Locate cells.
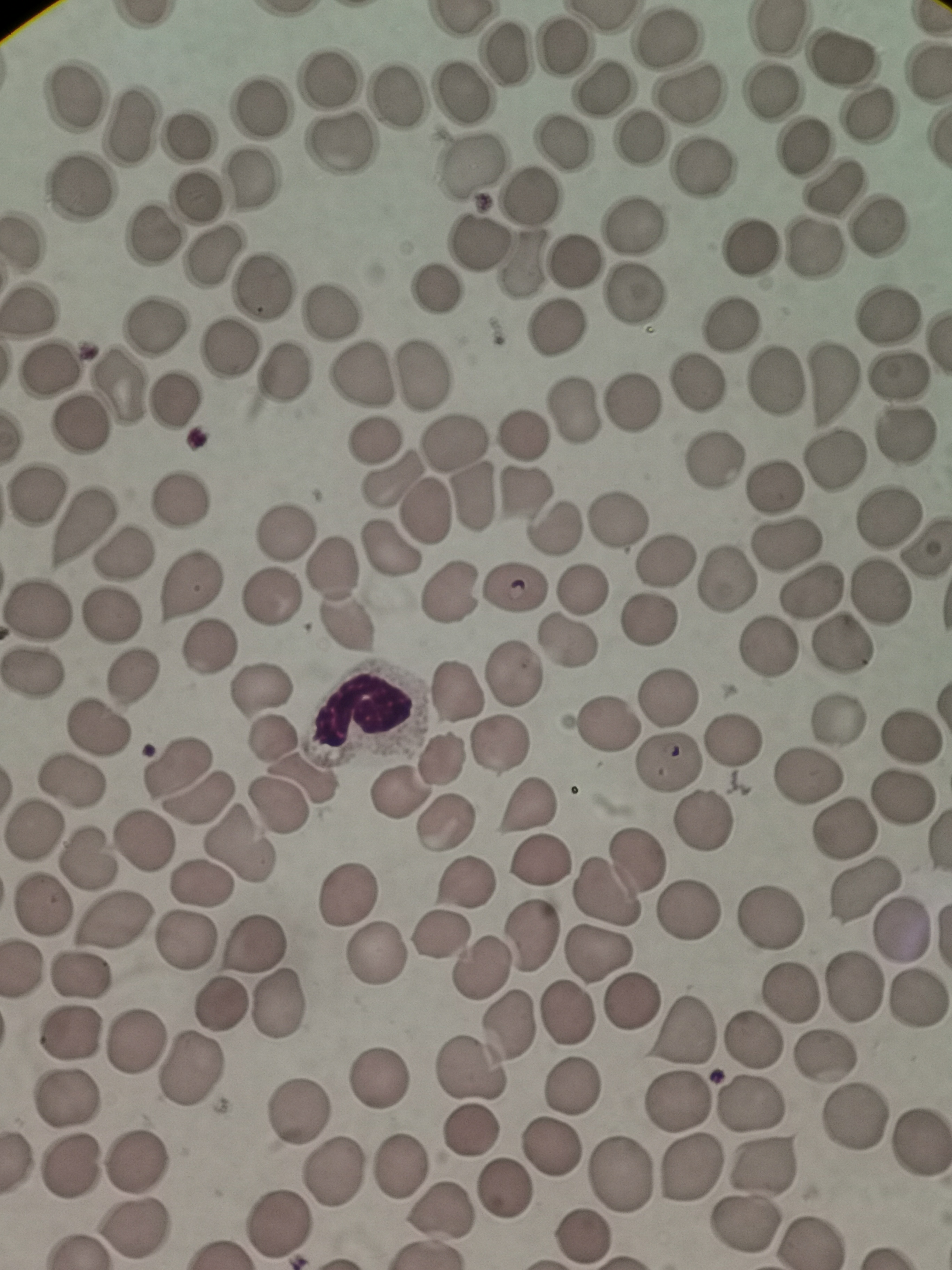
Approximate centers as (x, y) in pixels.
Cells: (775, 30), (665, 38), (564, 46), (507, 55), (842, 56), (330, 84), (605, 88), (772, 90), (399, 92), (467, 93), (694, 97), (78, 100), (264, 111), (871, 114), (130, 129), (637, 134), (193, 135), (340, 144), (563, 144), (801, 148), (473, 164), (702, 170), (253, 182), (82, 187), (833, 190), (530, 194), (199, 195), (634, 227), (880, 228), (150, 235), (483, 240), (750, 252), (817, 252), (210, 257), (575, 261), (525, 263), (259, 283), (433, 289), (631, 297), (29, 309), (334, 312), (886, 317), (155, 325), (731, 325), (558, 326), (228, 349), (53, 364), (424, 372), (280, 375), (897, 376), (362, 377), (774, 382), (831, 383), (696, 385), (118, 388), (175, 396), (629, 403), (572, 410), (80, 423), (903, 432), (523, 434), (453, 440), (372, 444), (833, 461), (714, 464), (392, 483), (776, 485), (474, 490), (32, 491), (181, 493), (523, 497), (426, 510), (887, 514), (618, 520), (85, 521), (559, 523), (286, 528), (786, 546), (390, 548), (926, 550), (126, 554), (336, 558), (667, 559), (727, 576), (185, 586), (582, 586), (515, 588), (812, 590), (449, 593), (881, 595), (273, 597), (38, 609), (109, 618), (651, 621), (348, 623), (565, 639), (844, 641), (208, 647), (763, 649), (34, 672), (514, 675), (134, 681), (259, 688), (459, 690), (666, 696), (835, 717), (606, 723), (99, 727), (272, 736), (913, 736), (732, 738), (497, 743), (439, 759), (669, 760), (174, 765), (806, 774), (303, 777), (73, 781), (397, 795), (901, 797), (200, 799), (527, 805), (280, 808), (705, 818), (448, 821), (842, 826), (35, 831), (145, 843), (242, 846), (87, 857), (543, 860), (620, 872), (464, 880), (202, 885), (864, 889), (346, 899), (43, 907), (685, 912), (771, 917), (113, 921), (900, 930), (444, 932), (532, 936), (187, 941), (253, 945), (600, 953), (375, 956), (477, 969), (83, 975), (853, 987), (786, 996), (914, 997), (632, 1000), (275, 1002), (220, 1005), (569, 1014), (508, 1021), (70, 1031), (683, 1031), (132, 1040), (752, 1042), (826, 1057), (190, 1069), (474, 1072), (382, 1079), (575, 1082), (680, 1099), (70, 1101), (753, 1103), (297, 1107), (854, 1118), (468, 1134), (917, 1147), (552, 1148), (134, 1162), (761, 1163), (398, 1165), (71, 1167), (689, 1167), (620, 1173), (336, 1177), (505, 1186), (440, 1210), (277, 1223), (747, 1224), (134, 1228), (583, 1234).

stain = Giemsa
capture = smartphone camera at the microscope eyepiece
image size = 952×1270 pixels
preparation = thin smear
field of view = single